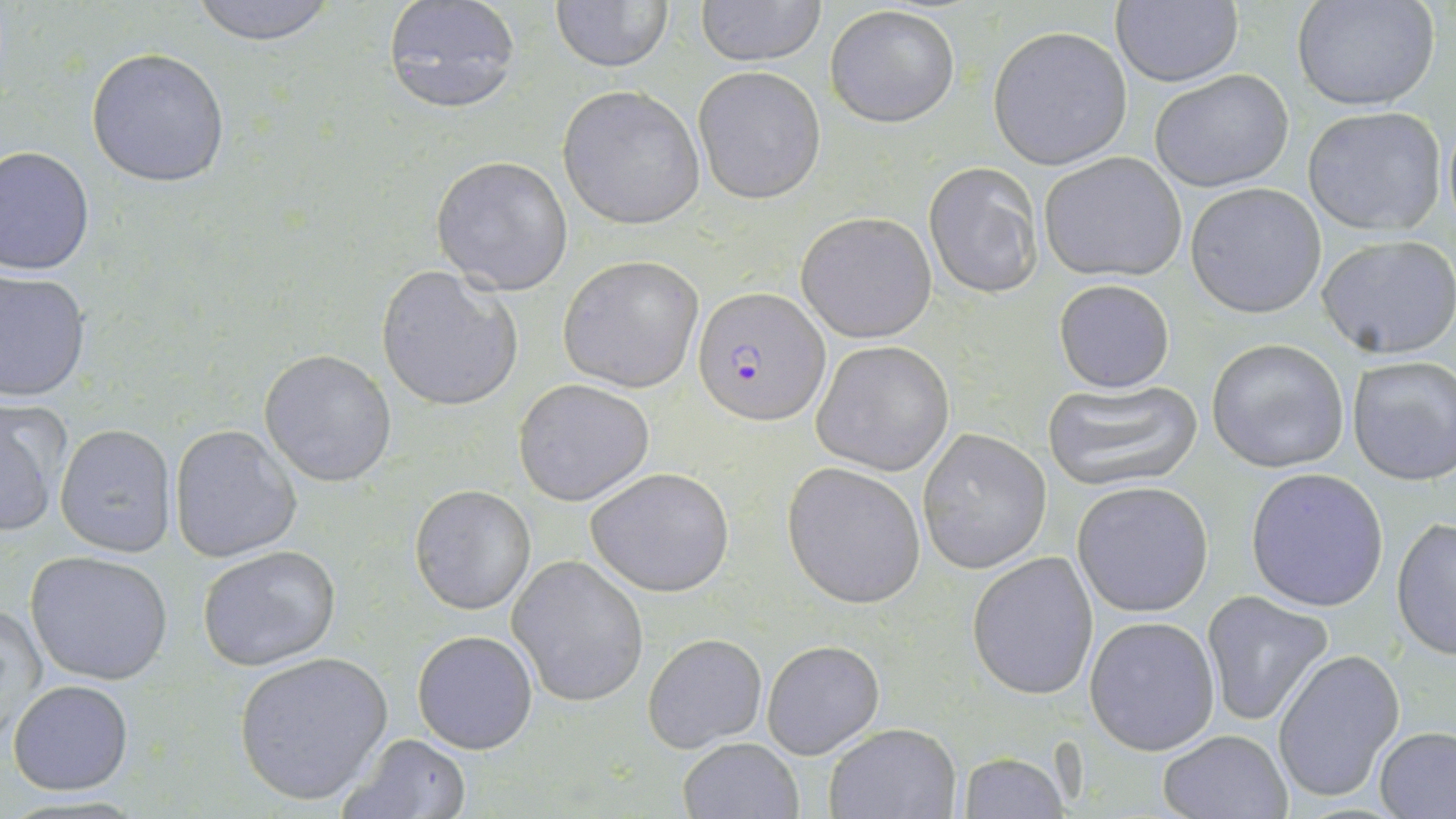

slide-level diagnosis = Plasmodium falciparum
preparation = thin blood smear
Plasmodium falciparum-infected red blood cell locations = approximate bounding boxes as [x1, y1, x2, y2] in pixels: [692, 285, 829, 426]
stain = May-Grünwald-Giemsa
image size = 1456×819 pixels
field of view = single
magnification = 1000x
uninfected red blood cell locations = approximate bounding boxes as [x1, y1, x2, y2] in pixels: [183, 0, 346, 45], [691, 0, 828, 66], [1290, 0, 1440, 113], [378, 1, 522, 114], [546, 1, 674, 75], [1109, 2, 1244, 87], [824, 4, 959, 128], [987, 26, 1134, 169], [85, 47, 231, 188], [693, 67, 826, 204], [1150, 69, 1295, 192], [557, 85, 705, 230], [1302, 108, 1445, 236], [1, 145, 96, 276], [1039, 151, 1189, 282], [430, 156, 573, 294], [923, 163, 1044, 300], [1185, 183, 1328, 319], [796, 211, 936, 343], [1317, 234, 1456, 359], [557, 254, 704, 395], [376, 265, 521, 412], [0, 269, 92, 401], [1052, 279, 1176, 393], [1206, 337, 1351, 473], [812, 340, 955, 476], [260, 349, 399, 486], [1346, 355, 1456, 486], [1043, 378, 1203, 491], [513, 379, 654, 505], [0, 400, 70, 540], [55, 423, 177, 559], [168, 424, 302, 563], [918, 426, 1053, 575], [781, 462, 927, 609], [585, 467, 735, 597], [1245, 468, 1390, 612], [1072, 480, 1213, 617], [409, 483, 536, 615], [1391, 517, 1456, 659], [197, 545, 341, 670], [24, 549, 175, 686], [966, 551, 1098, 699], [507, 555, 649, 707], [1199, 590, 1335, 727], [3, 599, 48, 747], [1084, 616, 1221, 755], [412, 629, 539, 754], [642, 633, 766, 753], [762, 639, 885, 759], [1273, 649, 1405, 805], [234, 650, 395, 807], [7, 680, 135, 794], [823, 723, 961, 819], [1375, 727, 1456, 818], [1157, 729, 1291, 818], [336, 734, 472, 819], [677, 737, 804, 819], [955, 751, 1069, 818]
modality = optical microscopy